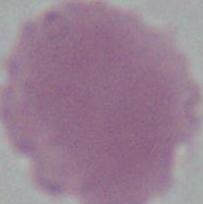

Summary:
  - Magnification: 1000x
  - Identification: erythrocyte
  - Modality: photomicrograph